Name the parasite shown.
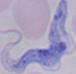
A trypanosome.

Summary:
  - Magnification: 1000x
  - Modality: photomicrograph